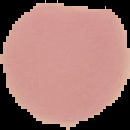 Image is 130×130 pixels. Segmented cell region on a black background. From a thin blood smear. Result: negative for Plasmodium parasites.